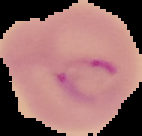
Summary:
  - Image size: 142×136 pixels
  - Image type: segmented cell region with the area outside set to black
  - Malaria status: parasitized
  - Preparation: thin blood smear